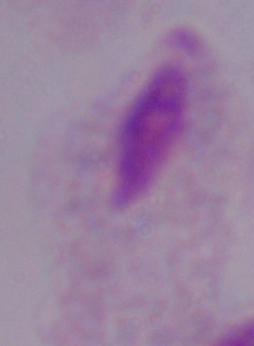

Summary:
  - Modality: micrograph
  - Identification: trichomonad
  - Magnification: 1000x